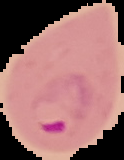

Summary:
  - Preparation: thin blood film
  - Image type: segmented cell region on a black background
  - Malaria status: parasitized
  - Image size: 124×160 pixels